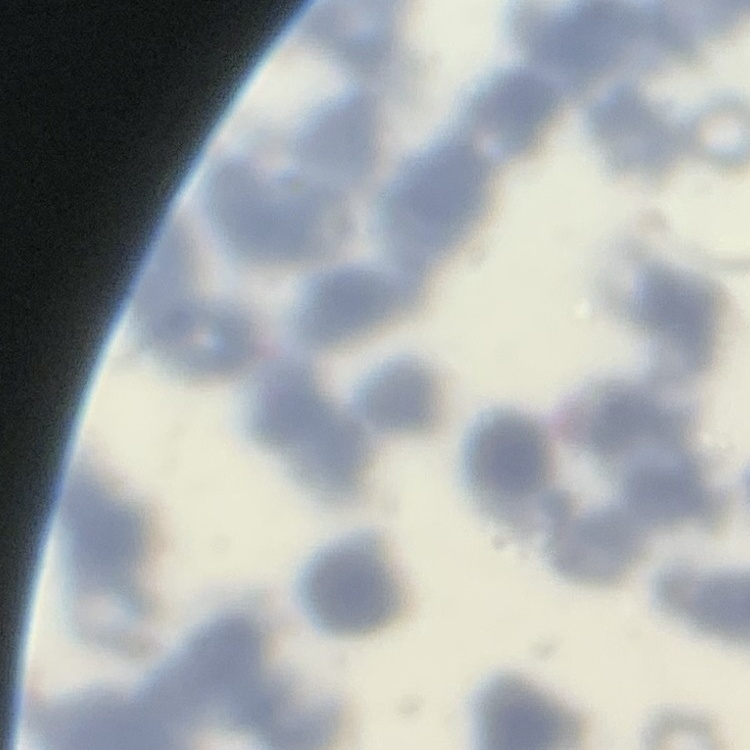
red blood cell morphology = rouleaux formation
stain = Field's or Giemsa
image type = square crop of a larger photomicrograph
preparation = thin peripheral smear